Give the extent of all uninfected red blood cells.
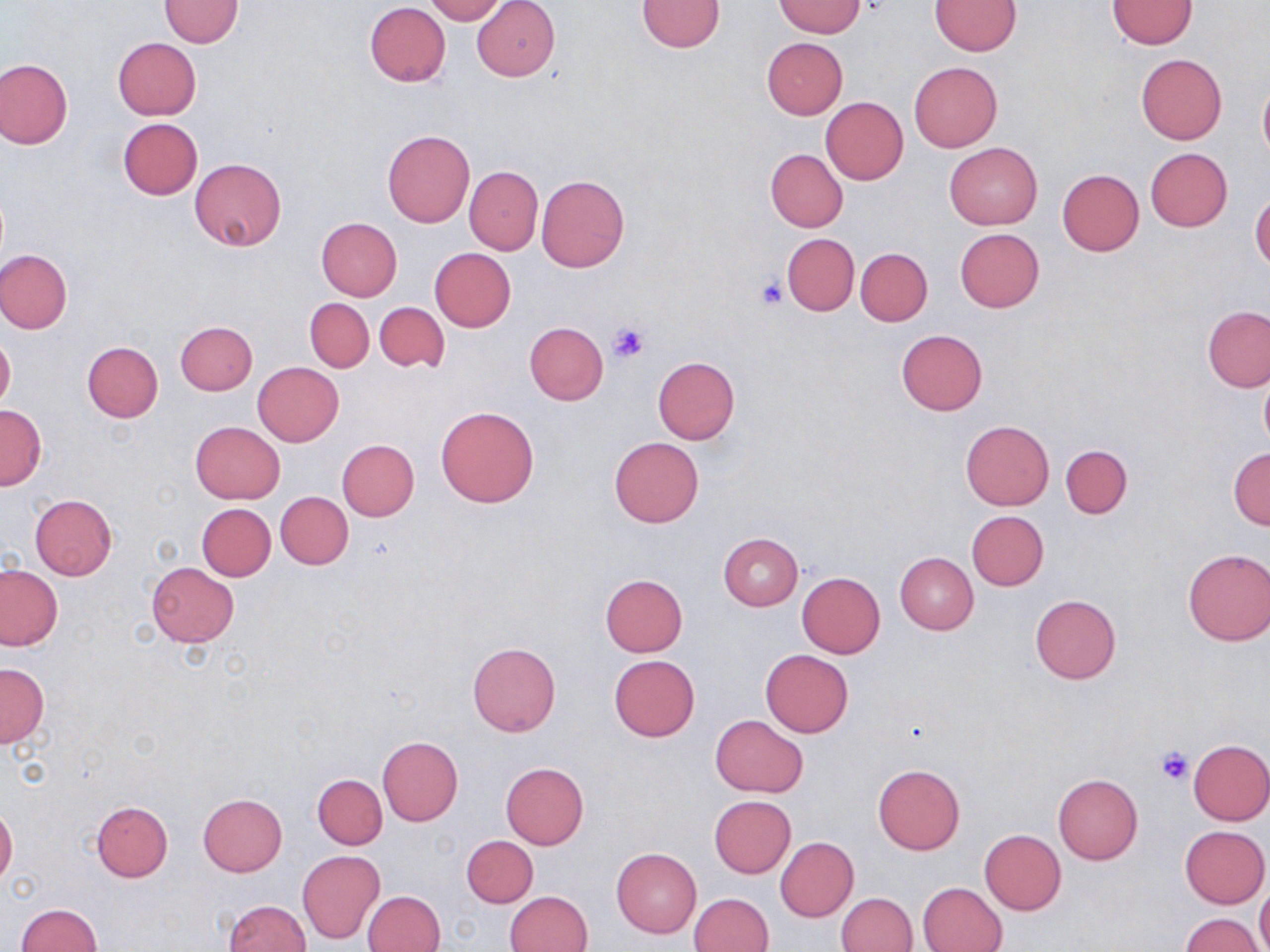
Approximate bounding boxes as named x1/y1/x2/y2 corners in pixels.
Uninfected red blood cells: (x1=423, y1=0, x2=506, y2=23), (x1=471, y1=0, x2=561, y2=81), (x1=159, y1=1, x2=244, y2=48), (x1=637, y1=1, x2=723, y2=52), (x1=930, y1=1, x2=1020, y2=55), (x1=1106, y1=1, x2=1197, y2=49), (x1=775, y1=2, x2=867, y2=37), (x1=365, y1=3, x2=450, y2=86), (x1=114, y1=37, x2=201, y2=119), (x1=761, y1=37, x2=848, y2=118), (x1=1135, y1=53, x2=1227, y2=145), (x1=1, y1=58, x2=72, y2=148), (x1=909, y1=62, x2=1002, y2=152), (x1=1258, y1=76, x2=1270, y2=165), (x1=820, y1=98, x2=908, y2=184), (x1=117, y1=117, x2=204, y2=199), (x1=382, y1=129, x2=475, y2=227), (x1=944, y1=142, x2=1042, y2=229), (x1=1145, y1=148, x2=1232, y2=231), (x1=765, y1=149, x2=848, y2=231), (x1=190, y1=157, x2=286, y2=250), (x1=465, y1=167, x2=542, y2=254), (x1=1057, y1=168, x2=1144, y2=256), (x1=535, y1=175, x2=630, y2=273), (x1=1250, y1=191, x2=1270, y2=272), (x1=317, y1=217, x2=401, y2=300), (x1=955, y1=228, x2=1045, y2=312), (x1=781, y1=233, x2=859, y2=315), (x1=856, y1=247, x2=932, y2=325), (x1=0, y1=248, x2=73, y2=334), (x1=430, y1=248, x2=516, y2=331), (x1=305, y1=299, x2=374, y2=373), (x1=374, y1=301, x2=449, y2=374), (x1=1203, y1=306, x2=1270, y2=391), (x1=176, y1=321, x2=258, y2=395), (x1=525, y1=322, x2=608, y2=405), (x1=895, y1=330, x2=987, y2=415), (x1=0, y1=333, x2=15, y2=414), (x1=82, y1=342, x2=163, y2=422), (x1=653, y1=357, x2=739, y2=443), (x1=252, y1=362, x2=344, y2=446), (x1=1258, y1=370, x2=1270, y2=455), (x1=0, y1=405, x2=46, y2=490), (x1=435, y1=406, x2=539, y2=507), (x1=960, y1=420, x2=1055, y2=510), (x1=190, y1=421, x2=285, y2=503), (x1=609, y1=437, x2=704, y2=527), (x1=337, y1=439, x2=419, y2=521), (x1=1060, y1=444, x2=1132, y2=518), (x1=1229, y1=447, x2=1270, y2=528), (x1=275, y1=492, x2=353, y2=569), (x1=29, y1=494, x2=117, y2=579), (x1=196, y1=503, x2=275, y2=580), (x1=966, y1=511, x2=1049, y2=591), (x1=717, y1=533, x2=803, y2=611), (x1=1182, y1=548, x2=1270, y2=646), (x1=896, y1=553, x2=978, y2=634), (x1=146, y1=563, x2=238, y2=646), (x1=0, y1=564, x2=64, y2=651), (x1=797, y1=573, x2=885, y2=658), (x1=600, y1=574, x2=688, y2=656), (x1=1029, y1=594, x2=1121, y2=683), (x1=466, y1=642, x2=561, y2=737), (x1=760, y1=650, x2=853, y2=737), (x1=609, y1=655, x2=700, y2=741), (x1=0, y1=664, x2=48, y2=747), (x1=710, y1=714, x2=809, y2=798), (x1=376, y1=736, x2=463, y2=826), (x1=1187, y1=739, x2=1270, y2=825), (x1=500, y1=761, x2=589, y2=849), (x1=872, y1=764, x2=964, y2=854), (x1=313, y1=774, x2=387, y2=849), (x1=1053, y1=775, x2=1144, y2=865), (x1=197, y1=794, x2=287, y2=876), (x1=709, y1=796, x2=796, y2=878), (x1=92, y1=800, x2=172, y2=881), (x1=0, y1=804, x2=18, y2=886), (x1=1179, y1=825, x2=1269, y2=908), (x1=979, y1=829, x2=1065, y2=914), (x1=462, y1=835, x2=538, y2=908), (x1=775, y1=836, x2=857, y2=922), (x1=612, y1=848, x2=701, y2=937), (x1=297, y1=849, x2=385, y2=944), (x1=918, y1=882, x2=1006, y2=951), (x1=1256, y1=882, x2=1270, y2=952), (x1=361, y1=890, x2=446, y2=952), (x1=505, y1=891, x2=593, y2=952), (x1=835, y1=892, x2=917, y2=952), (x1=689, y1=893, x2=773, y2=952), (x1=222, y1=900, x2=310, y2=952), (x1=15, y1=904, x2=102, y2=952), (x1=1181, y1=913, x2=1263, y2=952).

slide-level diagnosis = no evidence of blood parasites
preparation = thin blood film
modality = light microscopy
image size = 1270×952 pixels
stain = May-Grünwald-Giemsa
field of view = single
magnification = 1000x
platelet locations = approximate bounding boxes as named x1/y1/x2/y2 corners in pixels: (x1=756, y1=276, x2=789, y2=310), (x1=607, y1=321, x2=651, y2=364), (x1=1154, y1=744, x2=1193, y2=784)